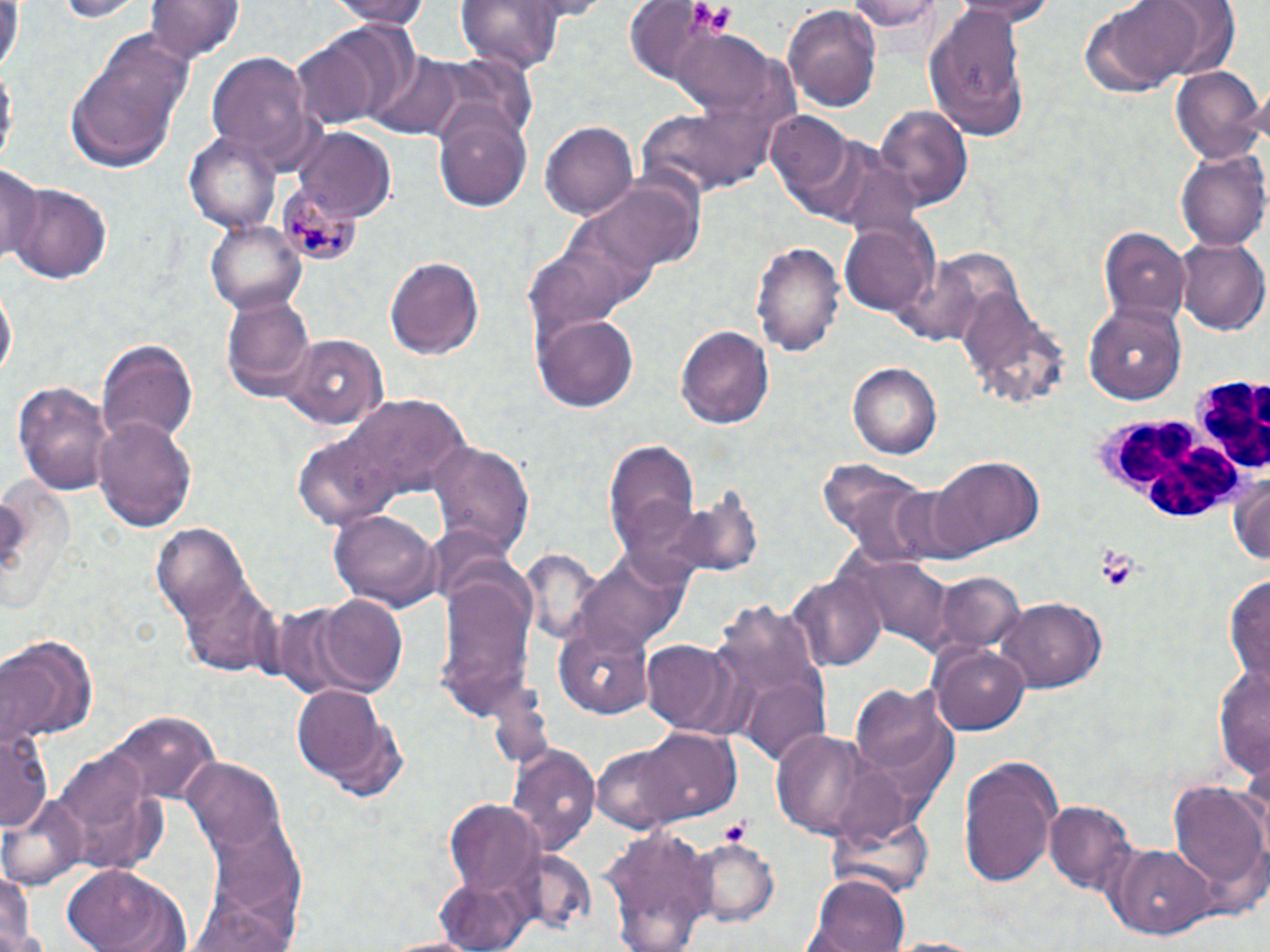

slide-level diagnosis = Plasmodium malariae
preparation = thin blood film
white blood cell locations = approximate bounding boxes as [x1, y1, x2, y2] in pixels: [1182, 376, 1270, 472], [1091, 419, 1251, 529]
image size = 1270×952 pixels
Plasmodium malariae-infected red blood cell locations = approximate bounding boxes as [x1, y1, x2, y2] in pixels: [275, 191, 355, 266]
platelet locations = approximate bounding boxes as [x1, y1, x2, y2] in pixels: [685, 4, 737, 37], [1096, 549, 1139, 591], [720, 818, 754, 843]
modality = optical microscopy
field of view = one of a larger specimen
uninfected red blood cell locations = approximate bounding boxes as [x1, y1, x2, y2] in pixels: [51, 0, 147, 22], [143, 0, 245, 63], [319, 0, 436, 25], [845, 0, 947, 36], [952, 0, 1063, 24], [1094, 0, 1210, 86], [1148, 0, 1241, 79], [0, 1, 23, 78], [452, 1, 576, 69], [627, 4, 764, 91], [783, 4, 883, 115], [922, 6, 1034, 141], [67, 29, 195, 173], [667, 29, 777, 113], [291, 30, 409, 132], [207, 48, 317, 169], [370, 51, 463, 140], [1, 62, 16, 172], [1169, 64, 1265, 162], [877, 104, 974, 210], [432, 107, 534, 215], [767, 113, 854, 198], [541, 120, 640, 219], [292, 129, 397, 220], [185, 132, 281, 232], [1177, 148, 1270, 250], [0, 162, 42, 266], [585, 171, 705, 271], [8, 181, 114, 284], [205, 217, 308, 313], [838, 222, 935, 317], [1097, 224, 1190, 323], [1174, 237, 1268, 335], [751, 238, 844, 357], [384, 252, 486, 360], [2, 279, 17, 385], [222, 290, 316, 402], [1084, 301, 1186, 404], [532, 313, 639, 413], [676, 323, 774, 431], [281, 333, 388, 430], [97, 337, 198, 449], [848, 361, 941, 459], [10, 379, 114, 495], [329, 394, 475, 508], [94, 413, 198, 532], [604, 437, 700, 567], [426, 439, 535, 560], [931, 456, 1045, 557], [1229, 467, 1270, 569], [0, 474, 78, 620], [327, 509, 442, 611], [151, 524, 281, 676], [571, 545, 690, 655], [436, 565, 538, 725], [927, 570, 1027, 659], [788, 571, 884, 673], [1225, 575, 1270, 684], [309, 593, 409, 697], [1000, 596, 1106, 694], [554, 624, 656, 719], [0, 633, 97, 744], [641, 640, 738, 734], [932, 643, 1031, 735], [1212, 659, 1270, 781], [741, 671, 833, 770], [851, 682, 952, 789], [294, 683, 391, 785], [101, 708, 221, 808], [2, 722, 52, 830], [771, 728, 887, 840], [639, 729, 741, 824], [587, 744, 693, 834], [509, 746, 598, 855], [54, 751, 169, 875], [958, 754, 1065, 888], [183, 758, 288, 856], [1168, 777, 1268, 909], [1, 794, 87, 888], [444, 798, 544, 901], [1045, 801, 1138, 894], [602, 824, 717, 952], [689, 837, 781, 926], [1106, 842, 1215, 938], [2, 860, 39, 952], [59, 865, 193, 952], [804, 875, 913, 952]
magnification = 1000x
stain = May-Grünwald-Giemsa